Identify the preparation type.
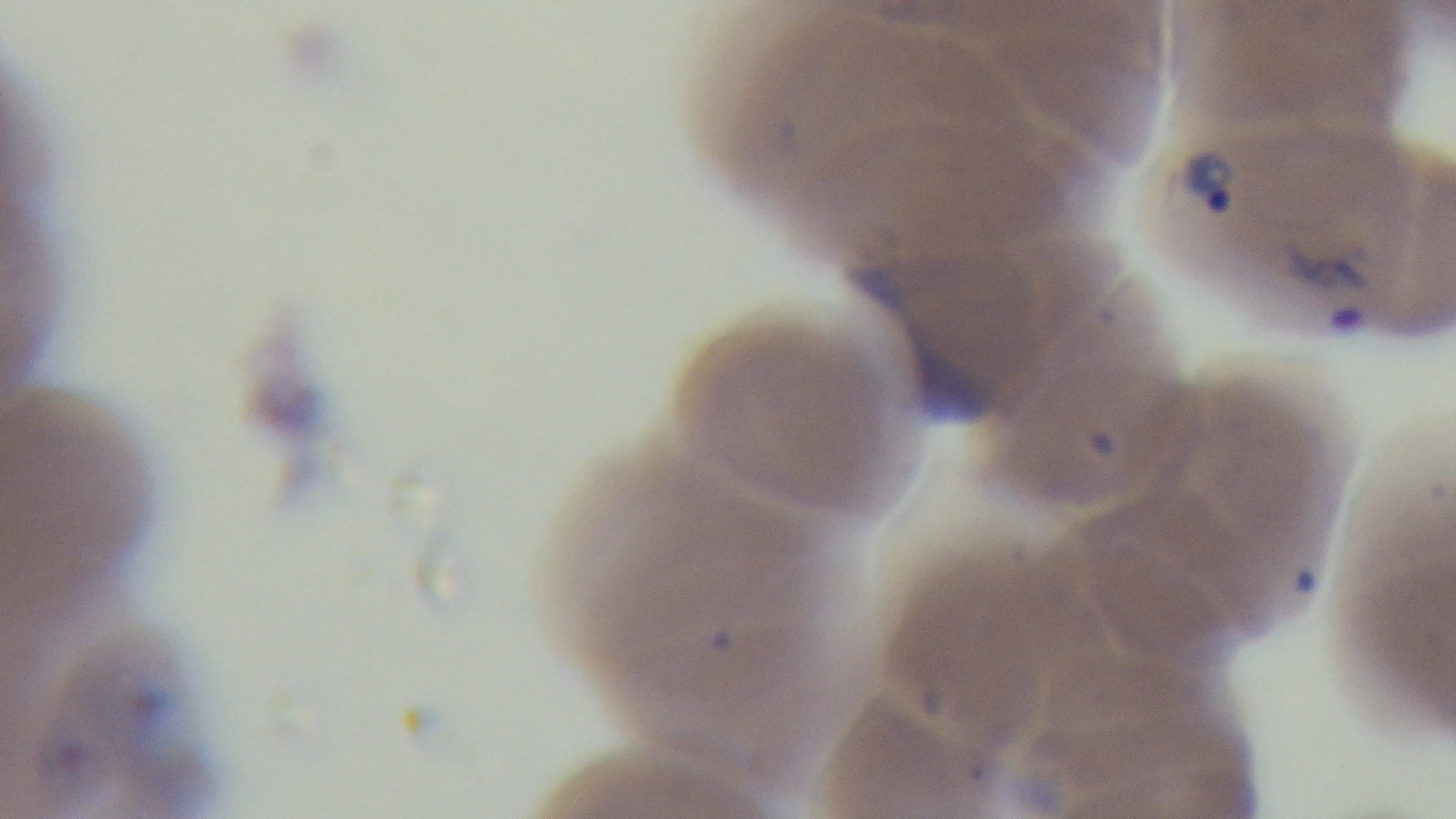

A thin smear.

Giemsa-stained. Malaria status: infected. 100x oil-immersion objective. One field from the slide. Light microscopy. Captured with a mounted 4K digital camera.